Locate every blood parasite and identify its species.
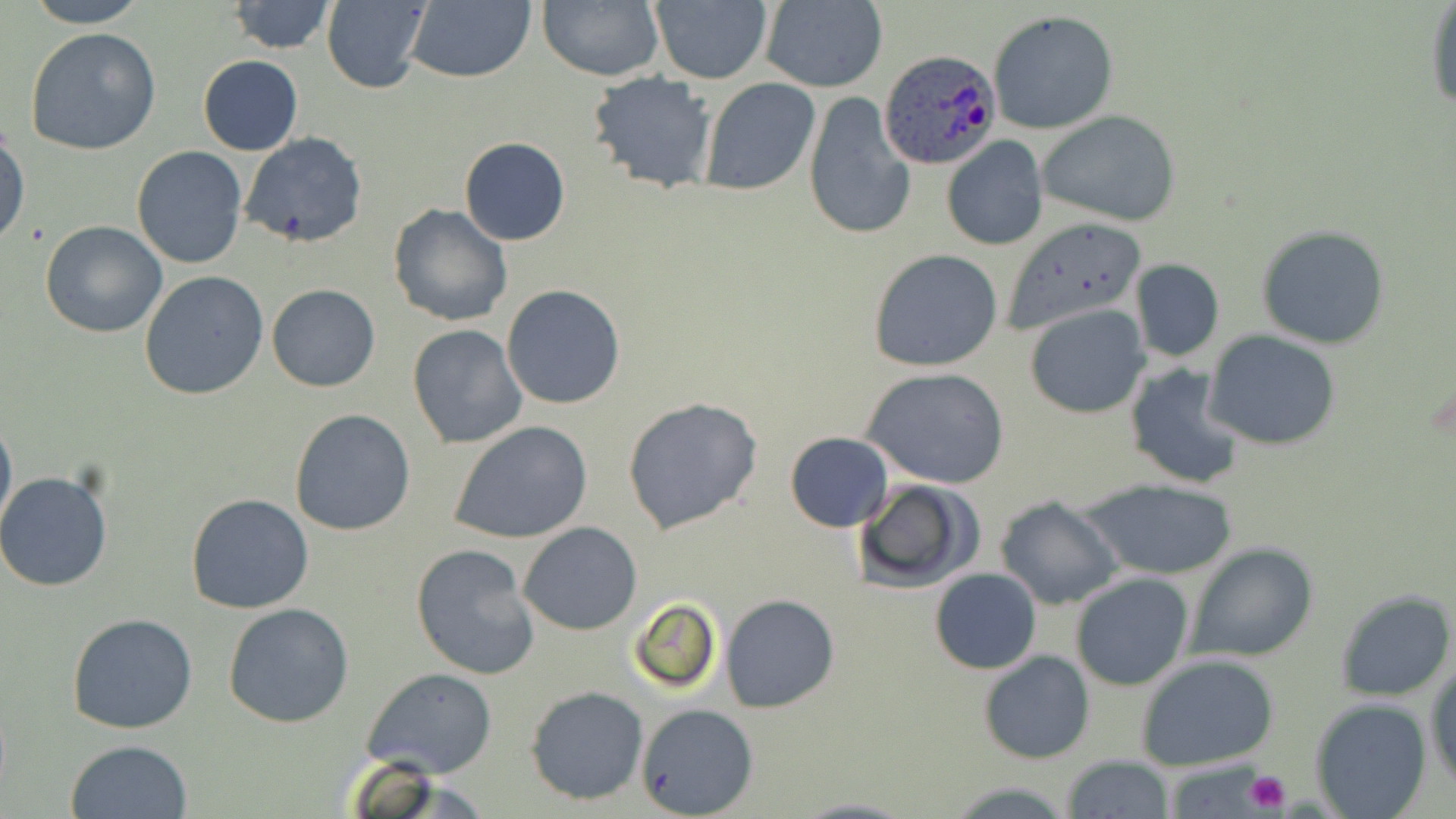
Approximate bounding boxes as (x1, y1, x2, y2) in pixels.
Plasmodium ovale-infected red blood cells: (881, 48, 1000, 169).
No Plasmodium falciparum, Plasmodium malariae, Plasmodium vivax, Babesia divergens, or Trypanosoma brucei observed.

{
  "slide_level_diagnosis": "Plasmodium ovale",
  "uninfected_red_blood_cell_locations": "approximate bounding boxes as (x1, y1, x2, y2) in pixels: (23, 0, 151, 27), (401, 0, 535, 84), (538, 0, 664, 81), (226, 1, 337, 53), (321, 1, 430, 92), (649, 1, 773, 84), (758, 1, 889, 92), (1425, 2, 1456, 113), (987, 10, 1118, 135), (26, 26, 163, 155), (198, 55, 303, 156), (586, 71, 718, 195), (699, 76, 820, 197), (802, 92, 915, 242), (1038, 110, 1181, 227), (0, 122, 30, 249), (238, 131, 369, 249), (940, 136, 1049, 253), (459, 137, 570, 246), (132, 146, 247, 268), (388, 203, 513, 327), (1002, 216, 1149, 336), (40, 219, 168, 337), (1259, 227, 1388, 350), (868, 248, 1003, 372), (1129, 258, 1225, 363), (139, 271, 270, 399), (267, 284, 380, 392), (501, 284, 628, 410), (1024, 303, 1149, 418), (407, 324, 527, 449), (1203, 330, 1341, 452), (1124, 362, 1246, 492), (863, 367, 1010, 491), (621, 395, 763, 535), (0, 408, 17, 539), (289, 408, 416, 536), (449, 420, 593, 544), (785, 431, 893, 530), (0, 469, 118, 594), (1081, 478, 1239, 581), (852, 479, 983, 593), (184, 491, 314, 614), (994, 493, 1124, 611), (518, 521, 641, 635), (410, 542, 542, 681), (1186, 543, 1318, 664), (930, 568, 1041, 675), (1071, 573, 1193, 691), (1335, 590, 1454, 699), (721, 594, 839, 712), (627, 597, 723, 696), (222, 602, 354, 727), (67, 611, 199, 735), (978, 650, 1095, 764), (1136, 655, 1281, 771), (1426, 663, 1456, 790), (362, 667, 497, 780), (525, 685, 650, 805), (1309, 697, 1432, 819), (637, 701, 757, 818), (66, 740, 194, 819), (1061, 756, 1176, 817), (789, 797, 919, 818)",
  "stain": "May-Grünwald-Giemsa",
  "image_size": "1456×819 pixels",
  "preparation": "thin blood smear",
  "modality": "light microscopy",
  "magnification": "1000x",
  "platelet_locations": "approximate bounding boxes as (x1, y1, x2, y2) in pixels: (1244, 770, 1292, 813)",
  "field_of_view": "one of a larger specimen"
}